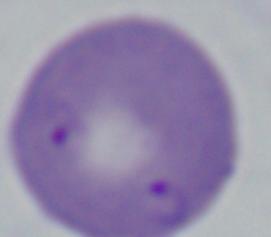

Summary:
  - Modality: photomicrograph
  - Magnification: 1000x
  - Identification: Babesia